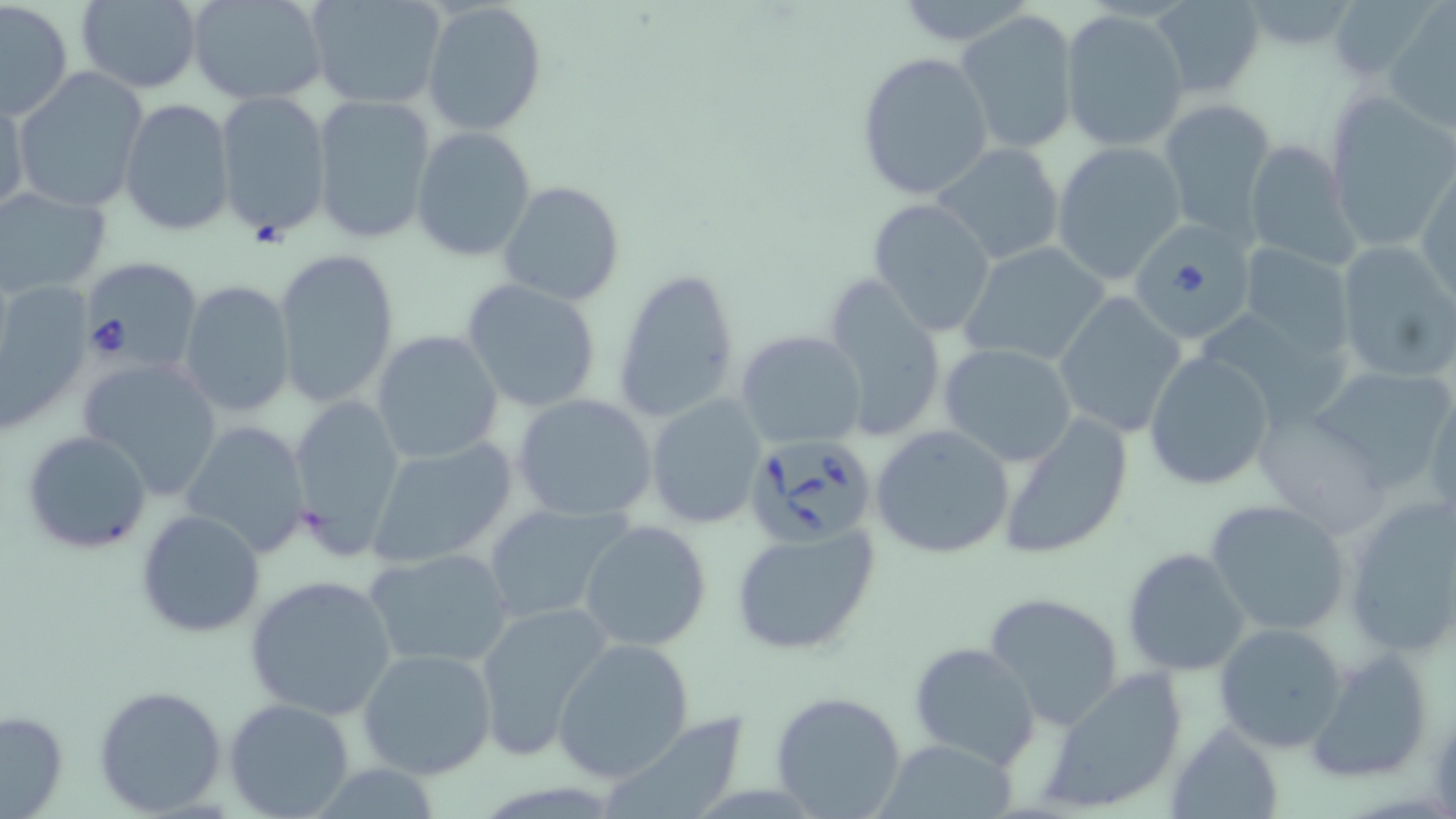
Summary:
  - Coordinate format: approximate bounding boxes as named x1/y1/x2/y2 corners in pixels
  - Babesia divergens-infected red blood cell locations: (x1=1134, y1=222, x2=1249, y2=340), (x1=74, y1=255, x2=201, y2=373), (x1=743, y1=431, x2=880, y2=545)
  - Uninfected red blood cell locations: (x1=74, y1=0, x2=202, y2=94), (x1=186, y1=0, x2=332, y2=106), (x1=308, y1=0, x2=449, y2=111), (x1=890, y1=0, x2=1039, y2=45), (x1=1150, y1=0, x2=1267, y2=97), (x1=421, y1=1, x2=547, y2=135), (x1=1, y1=2, x2=72, y2=119), (x1=1382, y1=4, x2=1456, y2=132), (x1=1060, y1=9, x2=1189, y2=152), (x1=953, y1=12, x2=1079, y2=152), (x1=855, y1=51, x2=995, y2=202), (x1=11, y1=68, x2=149, y2=214), (x1=214, y1=90, x2=333, y2=241), (x1=310, y1=90, x2=437, y2=244), (x1=1, y1=93, x2=28, y2=221), (x1=1325, y1=95, x2=1456, y2=250), (x1=119, y1=99, x2=236, y2=236), (x1=1159, y1=101, x2=1275, y2=237), (x1=410, y1=127, x2=538, y2=262), (x1=1242, y1=138, x2=1357, y2=269), (x1=1051, y1=141, x2=1186, y2=285), (x1=930, y1=142, x2=1067, y2=268), (x1=1416, y1=167, x2=1456, y2=304), (x1=498, y1=180, x2=625, y2=306), (x1=0, y1=186, x2=112, y2=300), (x1=867, y1=198, x2=997, y2=337), (x1=1335, y1=239, x2=1456, y2=384), (x1=959, y1=240, x2=1111, y2=368), (x1=1236, y1=242, x2=1358, y2=359), (x1=273, y1=247, x2=401, y2=409), (x1=611, y1=267, x2=742, y2=425), (x1=823, y1=277, x2=948, y2=442), (x1=0, y1=278, x2=91, y2=434), (x1=461, y1=278, x2=602, y2=413), (x1=179, y1=280, x2=298, y2=419), (x1=1053, y1=292, x2=1186, y2=438), (x1=735, y1=329, x2=869, y2=450), (x1=371, y1=330, x2=504, y2=464), (x1=938, y1=342, x2=1078, y2=466), (x1=1143, y1=351, x2=1277, y2=490), (x1=79, y1=356, x2=223, y2=498), (x1=1304, y1=363, x2=1456, y2=491), (x1=1425, y1=390, x2=1456, y2=520), (x1=512, y1=393, x2=659, y2=522), (x1=288, y1=394, x2=407, y2=554), (x1=645, y1=394, x2=767, y2=528), (x1=1252, y1=406, x2=1392, y2=532), (x1=996, y1=411, x2=1135, y2=560), (x1=179, y1=419, x2=309, y2=557), (x1=870, y1=424, x2=1015, y2=560), (x1=22, y1=429, x2=152, y2=554), (x1=366, y1=439, x2=517, y2=570), (x1=1340, y1=493, x2=1456, y2=660), (x1=1206, y1=498, x2=1353, y2=637), (x1=481, y1=502, x2=631, y2=624), (x1=135, y1=510, x2=266, y2=638), (x1=578, y1=519, x2=712, y2=651), (x1=728, y1=522, x2=882, y2=658), (x1=364, y1=547, x2=516, y2=670), (x1=1122, y1=547, x2=1251, y2=677), (x1=244, y1=575, x2=399, y2=720), (x1=982, y1=592, x2=1129, y2=731), (x1=475, y1=598, x2=614, y2=759), (x1=1213, y1=622, x2=1349, y2=752), (x1=551, y1=638, x2=696, y2=782), (x1=908, y1=641, x2=1042, y2=769), (x1=1307, y1=645, x2=1436, y2=782), (x1=358, y1=646, x2=497, y2=780), (x1=1036, y1=667, x2=1190, y2=816), (x1=94, y1=683, x2=227, y2=816), (x1=769, y1=690, x2=908, y2=819), (x1=223, y1=698, x2=356, y2=819), (x1=0, y1=708, x2=70, y2=818), (x1=601, y1=711, x2=750, y2=818), (x1=1169, y1=722, x2=1283, y2=819), (x1=875, y1=737, x2=1021, y2=818)
  - Slide-level diagnosis: Babesia divergens
  - Image size: 1456×819 pixels
  - Preparation: thin blood film
  - Modality: light microscopy
  - Field of view: one of a larger specimen
  - Stain: May-Grünwald-Giemsa
  - Magnification: 1000x